Point out every Plasmodium parasite.
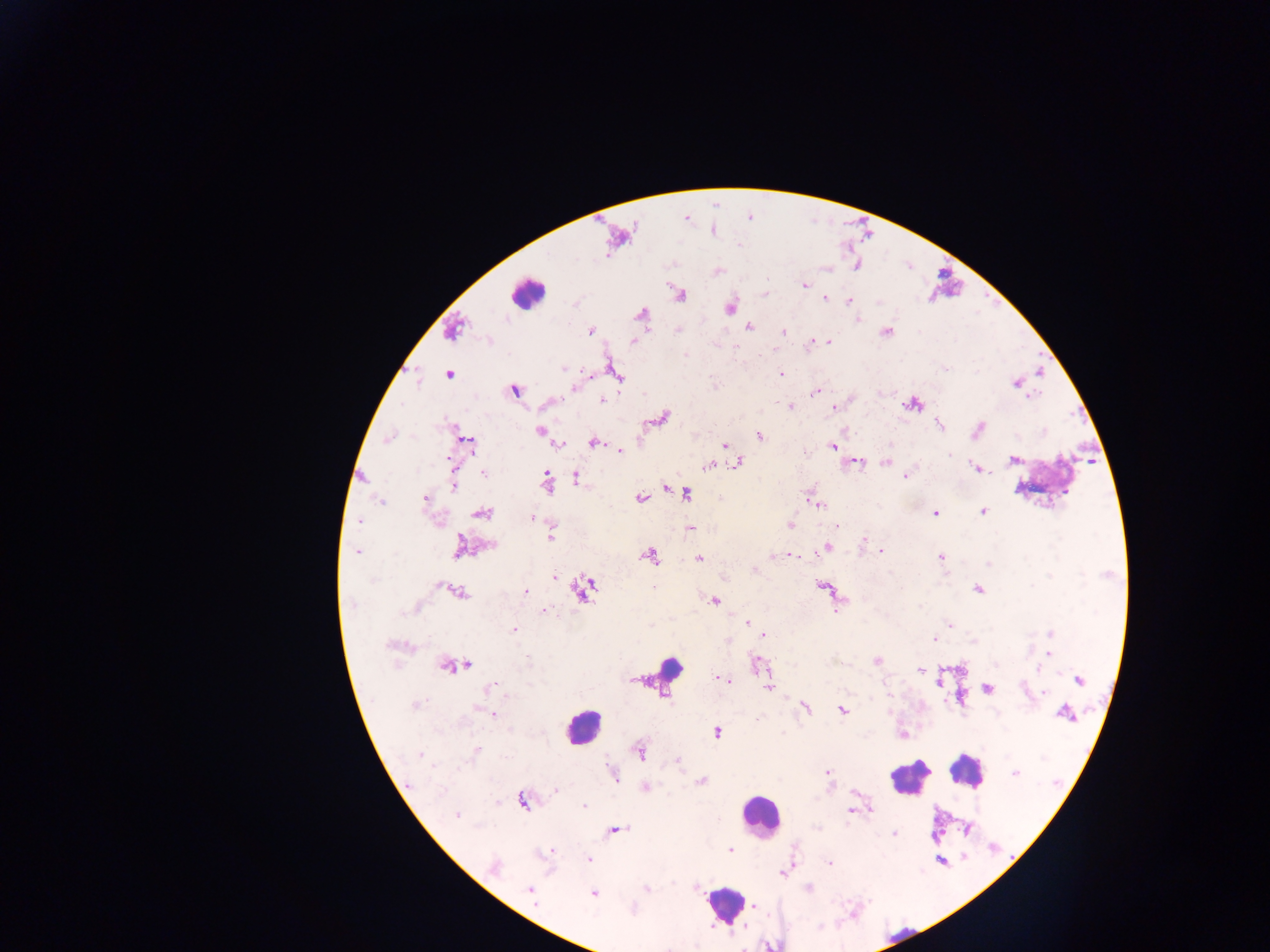
Approximate centers as x y in pixels.
Plasmodium parasites: 804 285; 825 299; 849 300; 730 308; 858 319; 748 327; 783 331; 591 332; 886 332; 633 341; 828 341; 812 342; 686 355; 563 368; 946 369; 448 374; 616 374; 780 374; 1017 383; 574 388; 514 390; 817 391; 602 401; 790 406; 834 407; 663 418; 938 425; 978 429; 540 430; 759 436; 388 438; 468 441; 592 442; 560 444; 725 445; 832 446; 620 450; 948 455; 1013 460; 450 462; 857 462; 885 462; 738 463; 708 465; 977 468; 483 474; 576 477; 905 477; 547 479; 454 486; 666 488; 686 494; 424 498; 641 498; 381 502; 818 505; 983 511; 481 512; 935 513; 532 517; 359 521; 790 526; 838 526; 690 528; 551 537; 863 539; 492 545; 460 546; 826 548; 819 550; 881 551; 357 553; 650 555; 790 555; 771 556; 940 557; 699 558; 988 564; 755 571; 554 577; 582 589; 978 590; 460 592; 525 592; 715 601; 353 604; 414 609; 543 610; 748 622; 950 625; 515 630; 1050 634; 764 635; 935 639; 727 640; 390 645; 1049 653; 877 660; 757 664; 466 665; 455 666; 919 669; 1037 669; 723 680; 1079 680; 939 681; 767 686; 490 688; 988 688; 1044 694; 415 705; 805 708; 842 711; 1064 713; 494 714; 718 733; 475 752; 640 753; 420 754; 678 762; 827 771; 1014 773; 614 775; 702 781; 409 785; 646 787; 555 790; 522 802; 584 806; 870 810; 850 811; 456 816; 616 830; 894 834; 730 849; 551 851; 588 859; 829 863; 495 867; 783 873; 809 888; 647 889; 530 890; 593 894; 754 906; 632 909.

leukocyte locations = approximate centers as x y in pixels: 527 294; 660 672; 582 726; 970 771; 908 778; 760 814; 723 904
field of view = single
image size = 1270×952 pixels
country = Ghana
preparation = thick blood smear
capture = mobile-phone photograph through a microscope